Outline each Plasmodium vivax-infected red blood cell.
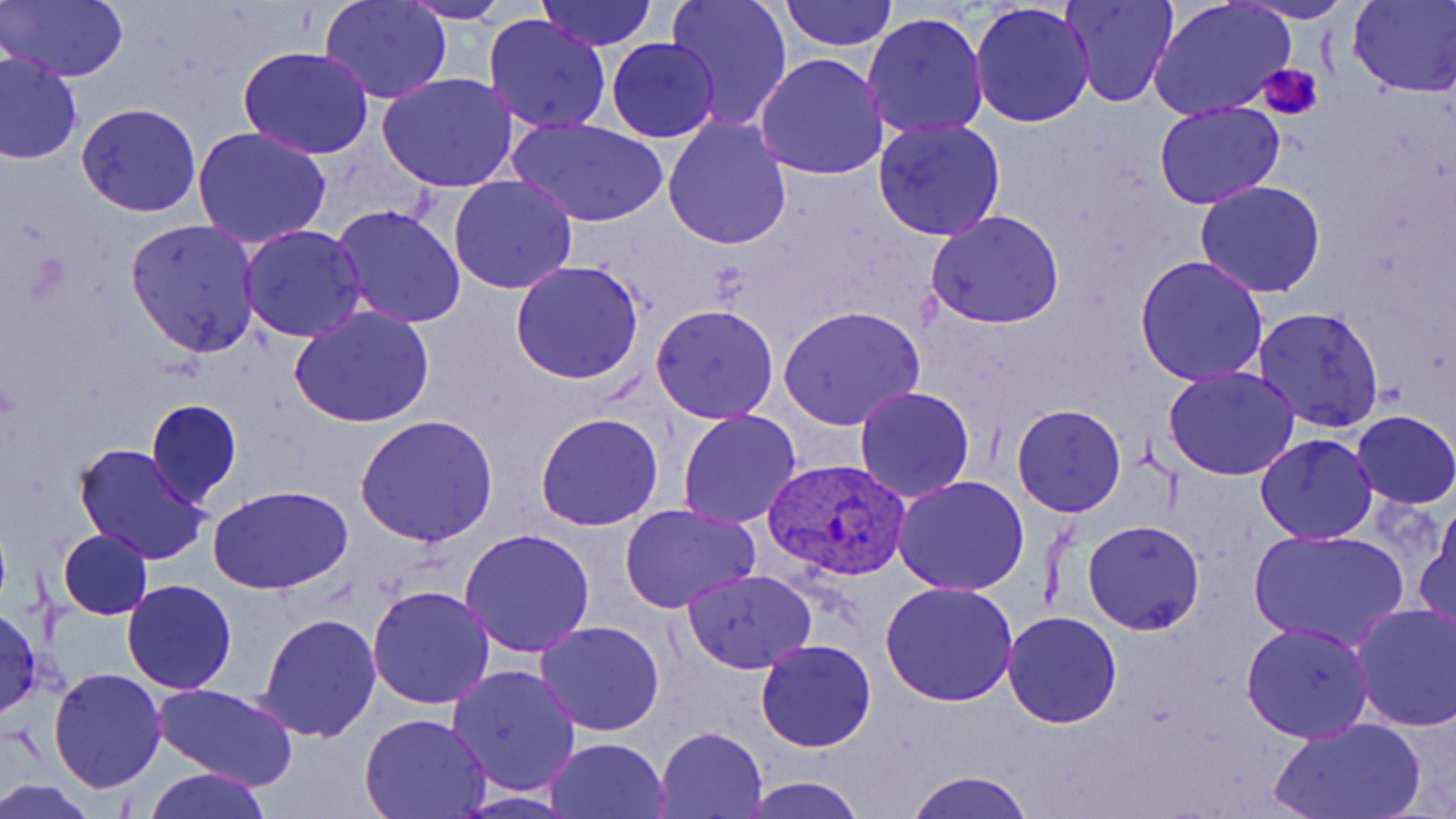

Approximate bounding boxes as (x1,y1)-(x2,y2) corner pairs in pixels.
Plasmodium vivax-infected red blood cells: (766,457)-(912,582).

slide_level_diagnosis: Plasmodium vivax
magnification: 1000x
field_of_view: single
image_size: 1456×819 pixels
uninfected_red_blood_cell_locations: 'approximate bounding boxes as (x1,y1)-(x2,y2) corner pairs in pixels: (3,0)-(128,83), (318,0)-(453,103), (538,0)-(656,51), (663,0)-(794,130), (780,0)-(898,50), (1060,0)-(1179,107), (1148,0)-(1296,122), (1348,0)-(1456,96), (1236,1)-(1358,23), (398,2)-(513,24), (969,2)-(1096,129), (861,11)-(989,138), (483,13)-(613,133), (606,36)-(720,143), (239,46)-(374,160), (0,53)-(82,164), (753,53)-(888,180), (375,73)-(521,192), (1153,100)-(1285,208), (77,103)-(201,218), (661,115)-(793,249), (506,116)-(670,228), (872,118)-(1007,240), (190,125)-(334,248), (448,174)-(579,294), (1195,181)-(1327,297), (331,205)-(467,329), (925,210)-(1067,330), (126,217)-(262,356), (239,224)-(368,342), (1134,255)-(1269,386), (511,261)-(644,385), (650,302)-(780,422), (291,306)-(436,428), (779,306)-(924,430), (1252,306)-(1385,432), (1162,364)-(1302,480), (854,385)-(976,502), (146,399)-(242,507), (1011,403)-(1126,518), (677,409)-(803,529), (1351,411)-(1455,509), (536,412)-(664,532), (354,413)-(499,547), (1255,433)-(1378,545), (73,443)-(212,567), (892,474)-(1029,595), (209,484)-(355,596), (619,502)-(760,614), (1415,512)-(1456,644), (1082,520)-(1206,635), (460,528)-(595,657), (1247,528)-(1408,652), (58,529)-(152,621), (683,568)-(816,673), (121,580)-(236,693), (881,581)-(1019,705), (367,585)-(496,709), (1350,601)-(1456,732), (0,605)-(42,720), (255,612)-(382,741), (1003,612)-(1122,729), (534,620)-(666,736), (1240,620)-(1373,742), (755,639)-(875,752), (446,663)-(582,797), (46,666)-(166,794), (153,682)-(301,790), (358,712)-(492,819), (1268,717)-(1428,819), (654,726)-(767,818), (544,737)-(670,819), (140,768)-(273,819), (904,771)-(1036,819), (738,777)-(867,818), (0,779)-(97,817)'
modality: light microscopy
preparation: thin blood smear
platelet_locations: 'approximate bounding boxes as (x1,y1)-(x2,y2) corner pairs in pixels: (1260,62)-(1324,119)'
stain: May-Grünwald-Giemsa